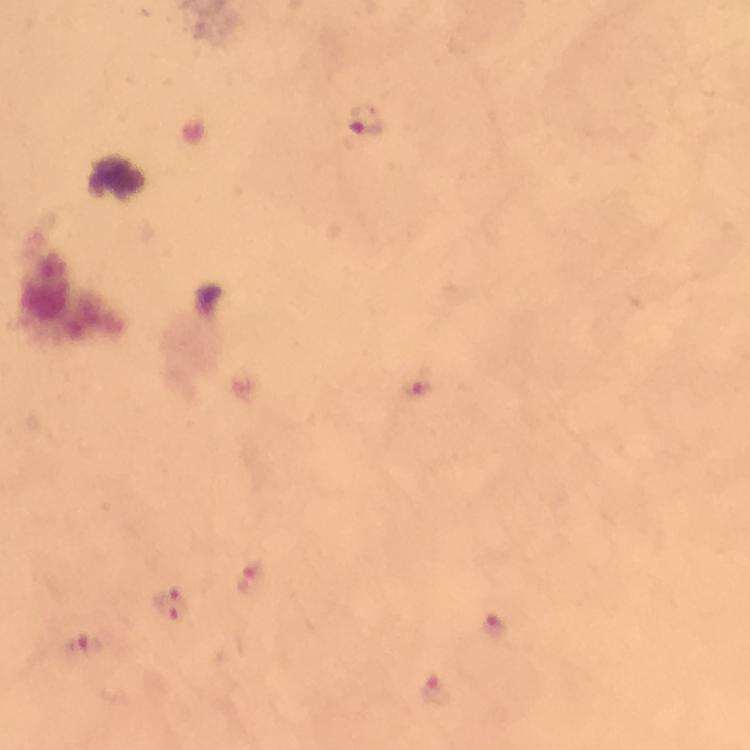
Approximate object centers, in pixels from the top-left corner.
Summary:
  - Malaria parasite locations: (x=364, y=120), (x=414, y=384), (x=253, y=577), (x=171, y=605), (x=492, y=626), (x=84, y=648), (x=438, y=690)
  - Cropped from: a single field of view
  - Stain: Giemsa
  - Immersion oil: applied
  - Preparation: thick smear
  - Image size: 750×750 pixels
  - Capture: smartphone photograph through a microscope
  - Magnification: 100x
  - Context: from a diagnostic examination for malaria